Report the malaria status of this cell.
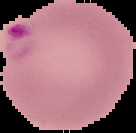

Parasitized.

Summary:
  - Image type: segmented cell region with the area outside set to black
  - Preparation: thin blood smear
  - Image size: 136×133 pixels